Name the parasite shown.
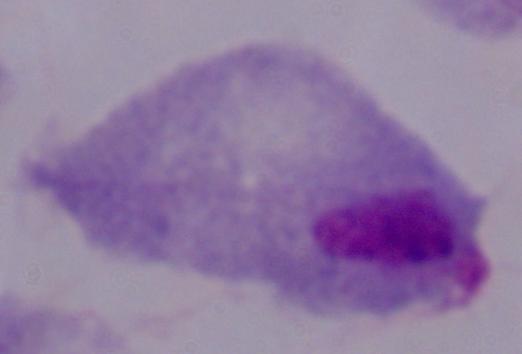
This is a trichomonad.

Captured at 1000x magnification. Micrograph.